Assess this cell for malaria.
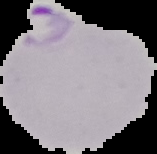

Parasitized.

The area outside the segmented cell region is set to black. Image is 157×154 pixels. From a thin blood film.